Identify the preparation type.
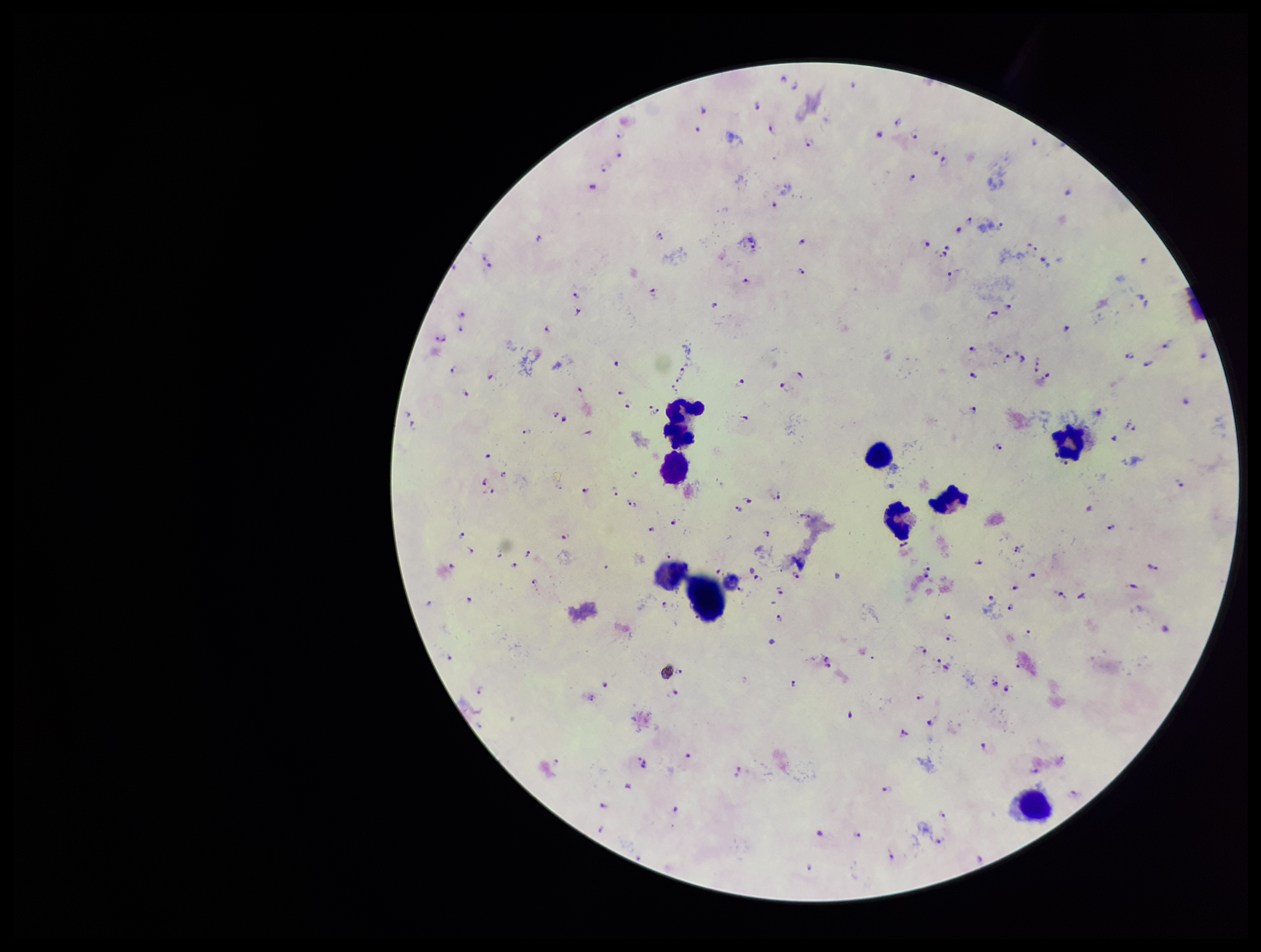
A thick smear.

field_of_view: one from this slide
leukocyte_count: 8
capture: smartphone photograph through the microscope eyepiece
patient_malaria_status: positive
species_reported_for_this_patient: Plasmodium falciparum
image_size: 1261×952 pixels
parasite_count: 133
stain: Giemsa
plasmodium_parasites: detected